Outline each uninfected red blood cell.
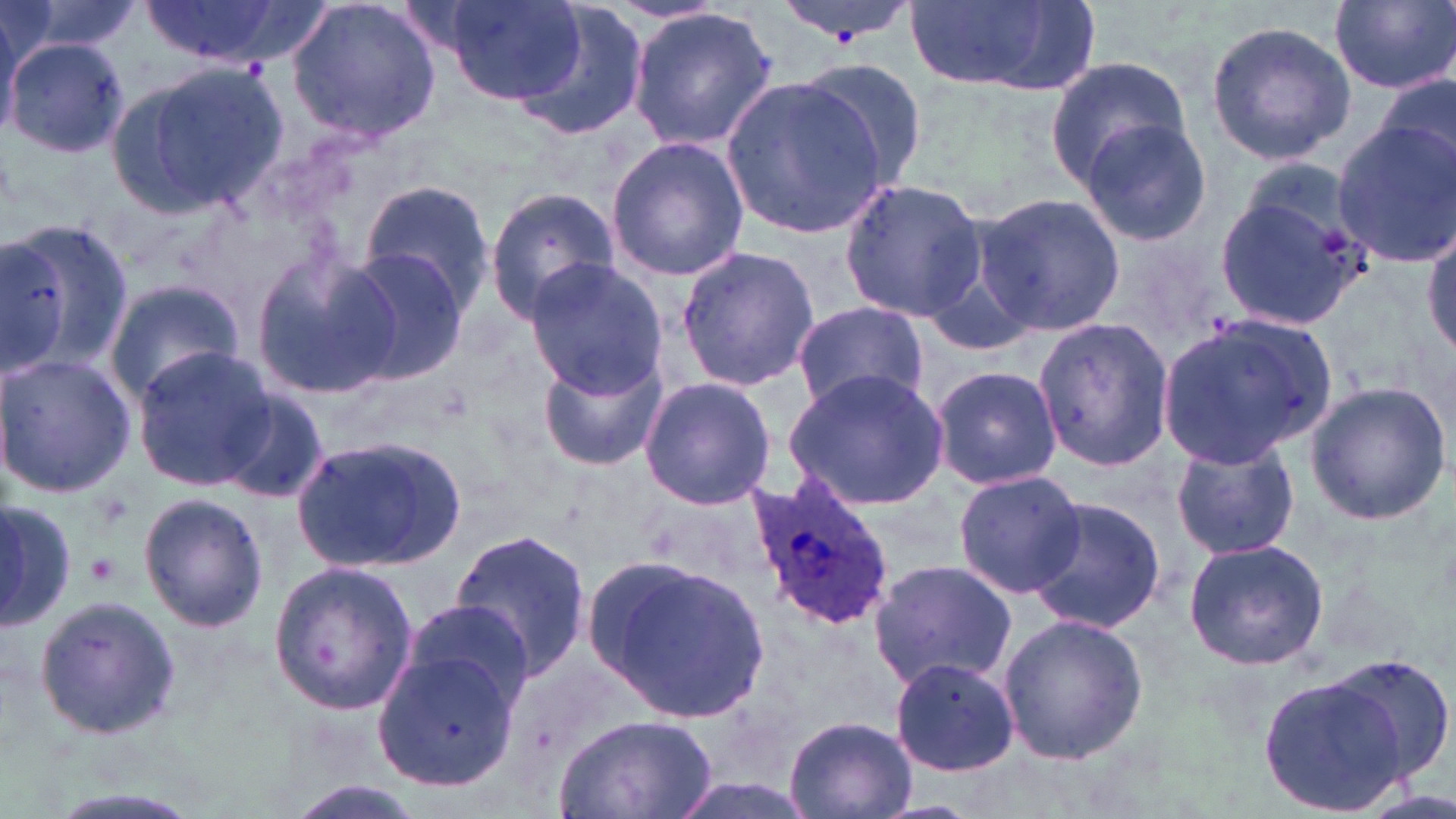
Approximate bounding boxes as [x1, y1, x2, y2] in pixels.
Uninfected red blood cells: [137, 0, 307, 65], [286, 0, 444, 143], [445, 0, 589, 105], [1329, 0, 1455, 94], [15, 1, 146, 57], [907, 2, 1094, 94], [0, 7, 21, 140], [507, 7, 650, 144], [628, 9, 779, 148], [1205, 19, 1355, 165], [2, 31, 123, 155], [1045, 59, 1196, 190], [113, 62, 287, 215], [798, 62, 931, 193], [1373, 70, 1456, 177], [723, 77, 888, 240], [1078, 115, 1214, 250], [1331, 119, 1456, 267], [606, 134, 749, 281], [838, 179, 989, 322], [359, 180, 495, 314], [1212, 181, 1367, 331], [485, 187, 618, 322], [972, 189, 1126, 340], [3, 217, 131, 378], [1424, 219, 1456, 361], [0, 238, 68, 378], [676, 246, 821, 394], [249, 247, 405, 398], [334, 248, 473, 386], [522, 260, 669, 394], [105, 279, 248, 406], [792, 299, 928, 414], [1032, 316, 1174, 474], [1153, 317, 1331, 471], [131, 346, 274, 492], [538, 351, 670, 471], [0, 352, 134, 498], [929, 365, 1062, 491], [784, 366, 950, 511], [637, 378, 776, 508], [1303, 381, 1451, 526], [218, 392, 330, 505], [291, 436, 465, 572], [1169, 436, 1299, 561], [952, 469, 1088, 597], [139, 492, 268, 633], [1025, 496, 1167, 635], [0, 500, 77, 634], [449, 528, 592, 681], [1182, 538, 1330, 672], [586, 552, 774, 724], [867, 556, 1017, 690], [266, 560, 419, 716], [33, 593, 183, 739], [402, 600, 534, 709], [997, 614, 1147, 766], [380, 634, 528, 794], [888, 656, 1021, 778], [1316, 656, 1456, 791], [1255, 674, 1414, 817], [555, 713, 717, 819], [783, 714, 916, 819], [277, 780, 427, 818].

Summary:
  - Platelet locations: [87, 552, 121, 586]
  - Plasmodium ovale-infected red blood cell locations: [746, 475, 894, 633]
  - Slide-level diagnosis: Plasmodium ovale
  - Image size: 1456×819 pixels
  - Field of view: one of a larger specimen
  - Preparation: thin blood film
  - Magnification: 1000x
  - Stain: May-Grünwald-Giemsa
  - Modality: light microscopy